Locate every uninfected red blood cell.
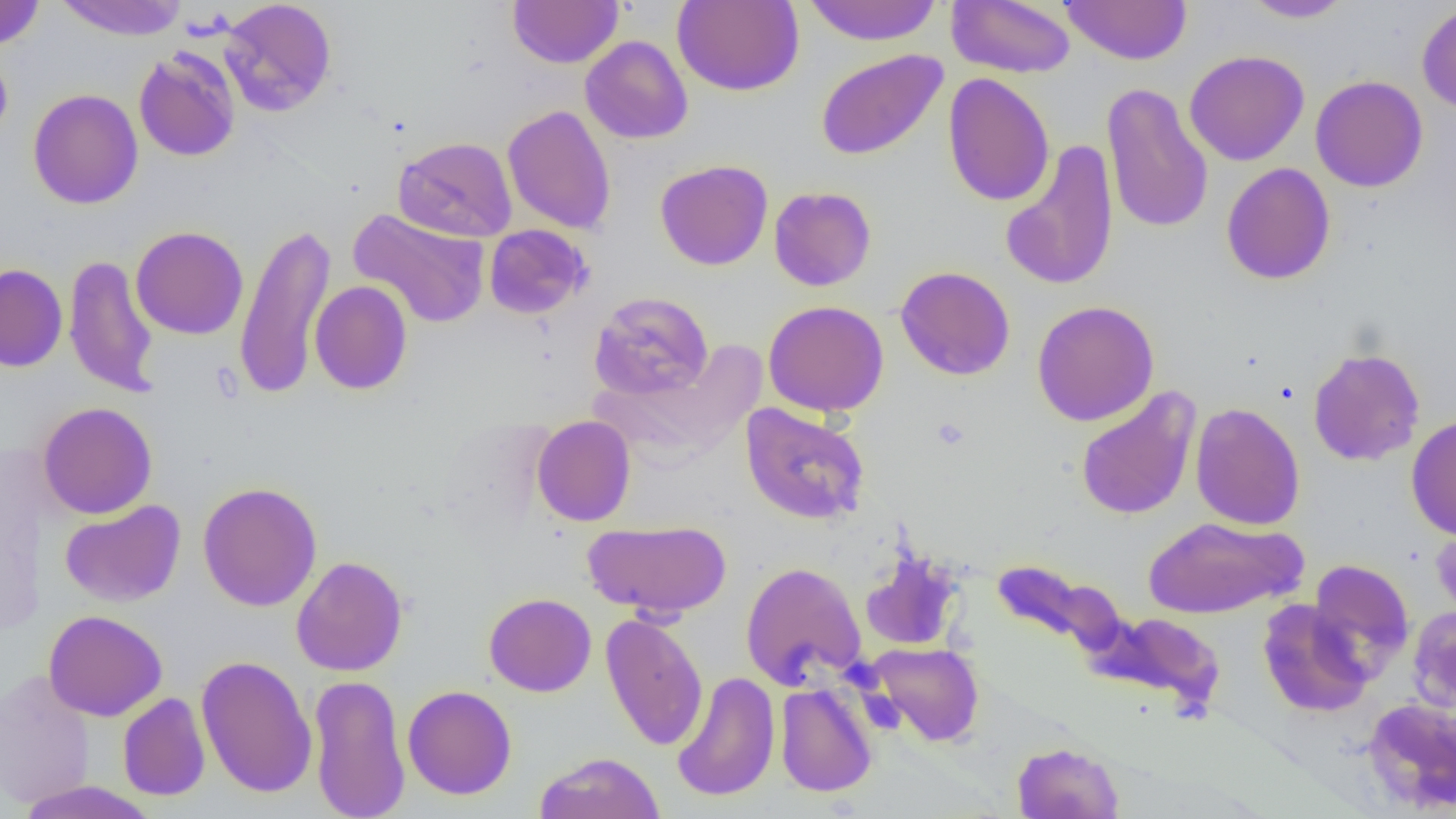

Approximate bounding boxes as [x1, y1, x2, y2] in pixels.
Uninfected red blood cells: [0, 0, 45, 50], [53, 0, 189, 40], [219, 0, 338, 116], [508, 0, 623, 68], [672, 0, 804, 96], [802, 0, 943, 45], [946, 0, 1076, 78], [1060, 0, 1193, 65], [1240, 0, 1356, 23], [1416, 3, 1456, 115], [580, 36, 693, 144], [0, 45, 13, 146], [133, 45, 241, 162], [815, 48, 948, 161], [1184, 50, 1309, 166], [942, 72, 1055, 207], [1310, 75, 1428, 193], [1102, 83, 1213, 234], [28, 88, 143, 209], [502, 104, 617, 235], [394, 136, 518, 242], [1000, 139, 1120, 291], [655, 159, 773, 270], [1221, 162, 1335, 285], [769, 186, 876, 291], [348, 208, 491, 329], [233, 223, 337, 400], [484, 224, 592, 319], [131, 226, 248, 339], [63, 254, 159, 398], [0, 264, 68, 372], [895, 265, 1015, 380], [310, 280, 412, 395], [587, 290, 714, 401], [763, 300, 889, 417], [1031, 300, 1160, 426], [1308, 347, 1425, 467], [1075, 387, 1201, 521], [38, 402, 158, 519], [740, 402, 870, 524], [1189, 402, 1305, 530], [1406, 414, 1456, 540], [531, 415, 636, 527], [197, 481, 323, 612], [60, 500, 186, 607], [1143, 516, 1305, 619], [583, 519, 732, 618], [1432, 521, 1456, 626], [859, 552, 964, 651], [291, 555, 408, 676], [992, 558, 1223, 719], [1308, 558, 1414, 677], [740, 561, 866, 689], [484, 593, 596, 697], [1257, 599, 1373, 717], [1407, 606, 1456, 714], [43, 610, 168, 721], [600, 612, 709, 751], [867, 642, 984, 747], [196, 654, 318, 798], [1, 668, 96, 810], [672, 672, 781, 802], [308, 673, 411, 819], [774, 682, 877, 798], [402, 685, 517, 800], [117, 692, 211, 801], [1363, 698, 1456, 813], [1012, 741, 1125, 819], [534, 751, 665, 819], [15, 781, 159, 819].

Summary:
  - Platelet locations: [930, 416, 972, 451]
  - Slide-level diagnosis: negative for blood parasites
  - Preparation: thin blood smear
  - Image size: 1456×819 pixels
  - Field of view: one of a larger specimen
  - Modality: optical microscopy
  - Magnification: 1000x